Assess this cell for malaria.
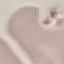

It is uninfected.

stain = Giemsa
image type = cell patch, automatically extracted from a larger field of view and resized to 64 × 64 pixels
preparation = thin smear
capture = smartphone through the microscope eyepiece